Classify this cell by malaria status.
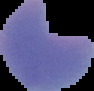

It is parasitized.

Summary:
  - Image size: 94×91 pixels
  - Preparation: thin blood film
  - Image type: cell region segmented out of the field of view; surrounding area masked to black